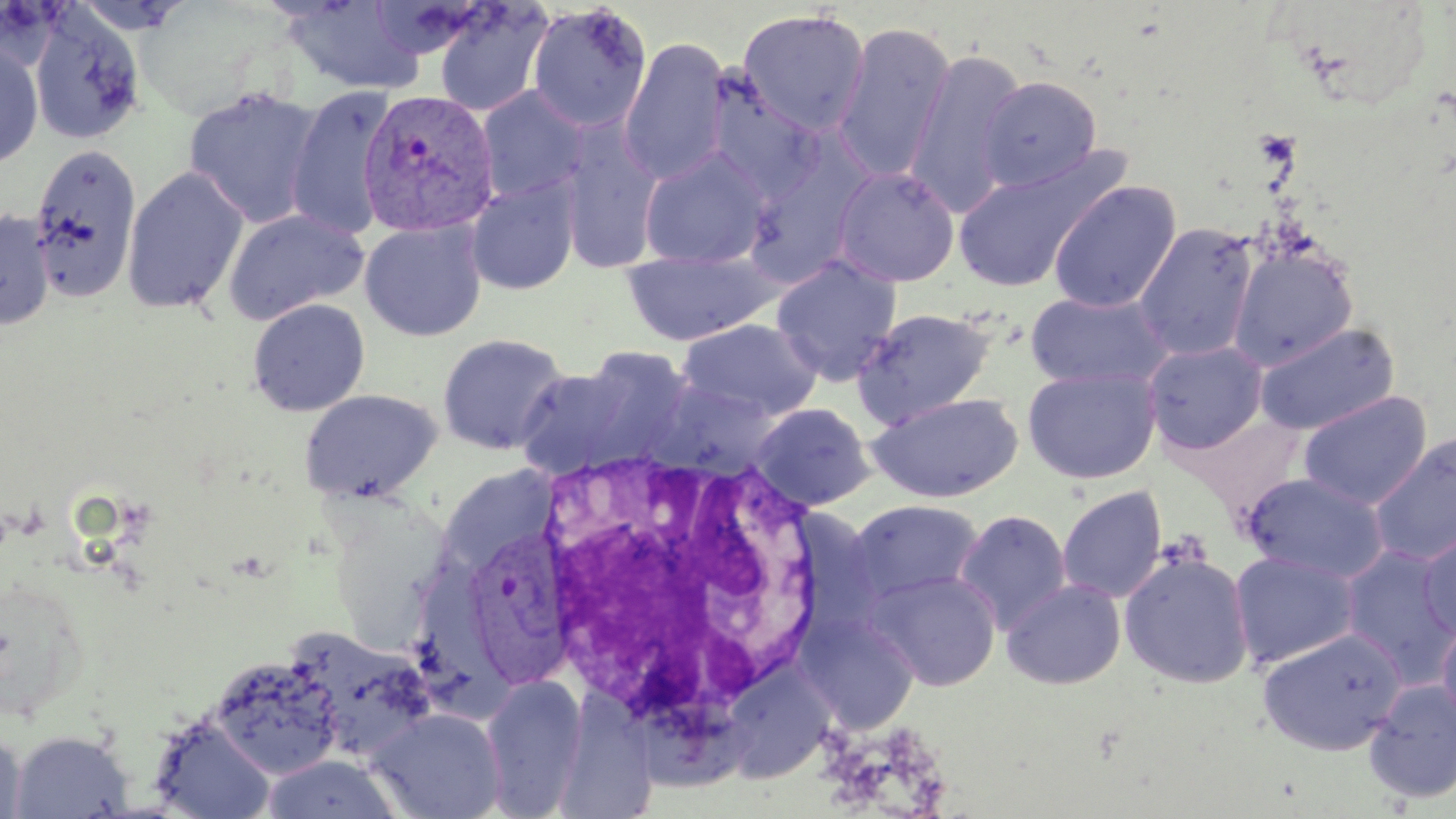
Summary:
  - Coordinate format: approximate bounding boxes as [x1, y1, x2, y2] in pixels
  - White blood cell locations: [529, 445, 834, 748]
  - Uninfected red blood cell locations: [135, 1, 275, 119], [280, 1, 425, 94], [433, 3, 552, 116], [525, 3, 652, 132], [737, 8, 871, 136], [29, 9, 145, 146], [831, 21, 956, 185], [619, 37, 730, 186], [0, 43, 43, 169], [904, 47, 1027, 216], [703, 74, 827, 201], [978, 75, 1102, 192], [286, 84, 396, 241], [476, 86, 587, 204], [183, 87, 324, 228], [557, 118, 662, 275], [30, 144, 142, 302], [638, 147, 772, 270], [742, 147, 874, 285], [950, 151, 1124, 294], [832, 165, 960, 287], [121, 166, 248, 313], [466, 176, 580, 295], [1048, 180, 1182, 313], [223, 208, 368, 326], [0, 210, 55, 330], [359, 220, 486, 341], [1135, 223, 1259, 361], [1228, 243, 1358, 370], [621, 247, 782, 346], [771, 254, 903, 386], [1025, 288, 1175, 391], [247, 298, 370, 416], [852, 307, 995, 427], [677, 318, 823, 420], [1253, 322, 1400, 436], [436, 332, 570, 454], [1143, 340, 1268, 455], [514, 351, 689, 480], [1022, 366, 1161, 484], [650, 380, 783, 476], [299, 388, 443, 502], [867, 391, 1023, 502], [1298, 391, 1432, 509], [749, 402, 877, 510], [1369, 432, 1456, 566], [440, 466, 559, 568], [1242, 472, 1390, 582], [1057, 486, 1167, 603], [848, 498, 985, 606], [953, 510, 1072, 634], [1418, 528, 1456, 639], [1340, 546, 1456, 684], [1119, 549, 1254, 689], [1229, 550, 1360, 669], [417, 552, 508, 718], [866, 569, 1002, 691], [1001, 578, 1126, 689], [798, 614, 920, 732], [1437, 616, 1456, 730], [1256, 625, 1406, 756], [294, 632, 437, 759], [208, 652, 344, 779], [723, 665, 834, 783], [481, 674, 588, 817], [1363, 678, 1456, 804], [559, 686, 649, 819], [616, 699, 761, 791], [368, 708, 507, 819], [148, 713, 275, 819], [0, 728, 27, 819], [9, 729, 133, 818], [260, 755, 403, 817]
  - Plasmodium vivax-infected red blood cell locations: [359, 90, 506, 237], [470, 531, 578, 695]
  - Slide-level diagnosis: Plasmodium vivax
  - Preparation: thin blood film
  - Modality: optical microscopy
  - Stain: May-Grünwald-Giemsa
  - Magnification: 1000x
  - Image size: 1456×819 pixels
  - Field of view: single